Assess for malaria.
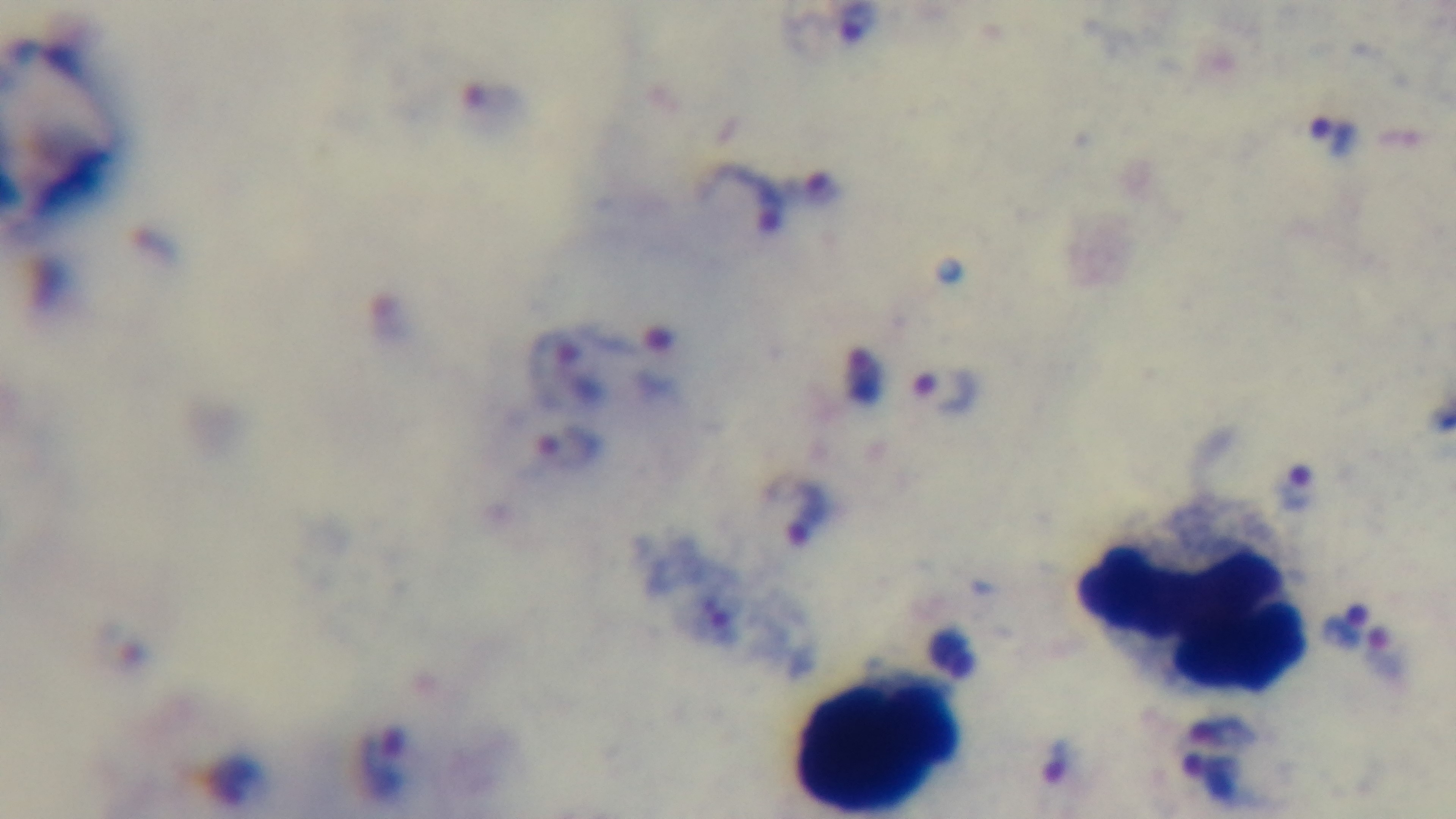
It is infected.

field of view = one from the slide
stain = Giemsa
modality = light microscopy
objective = 100x oil immersion
preparation = thick
capture = mounted 4K digital camera